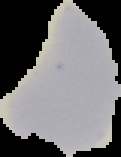
image size = 121×157 pixels
preparation = thin blood film
image type = segmented cell region on a black background
malaria status = uninfected